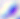

Summary:
  - Modality: micrograph
  - Identification: Toxoplasma gondii
  - Magnification: 400x